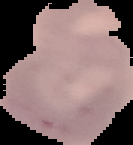
The area outside the segmented cell region is set to black. Image is 133×145 pixels. Result: no Plasmodium parasites detected. From a thin blood film.